Classify this cell by malaria status.
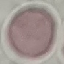

It is uninfected.

Summary:
  - Capture: smartphone camera at the microscope eyepiece
  - Preparation: thin blood smear
  - Image type: automatically extracted cell patch, resized to 64 × 64 pixels
  - Stain: Giemsa